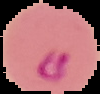
Result: malaria parasites detected. Segmented cell region on a black background. Image is 100×94 pixels. From a thin blood smear.